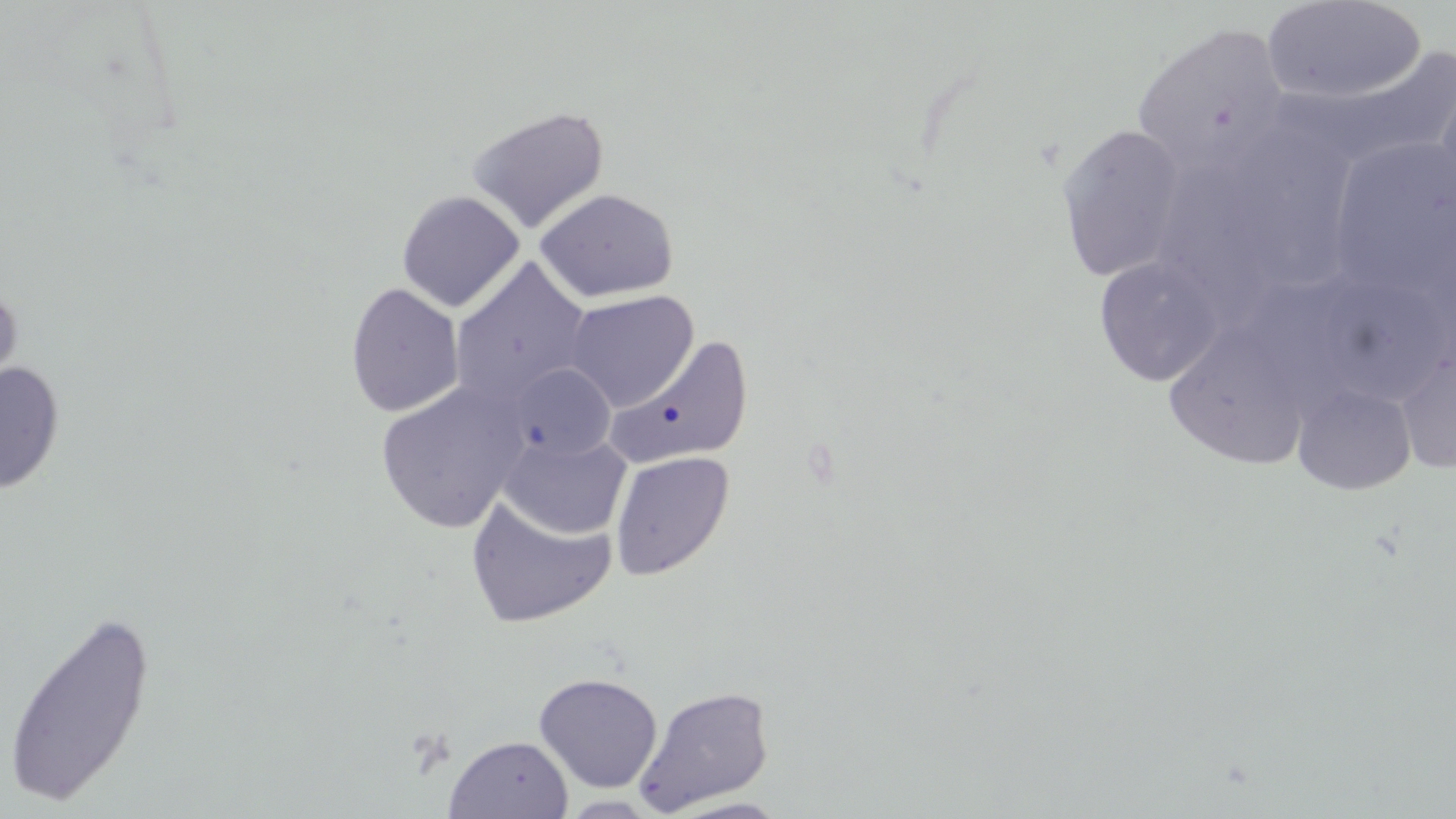
{
  "slide_level_diagnosis": "negative for blood parasites",
  "stain": "May-Grünwald-Giemsa",
  "preparation": "thin blood film",
  "image_size": "1456×819 pixels",
  "magnification": "1000x",
  "field_of_view": "one of a larger specimen",
  "modality": "optical microscopy",
  "uninfected_red_blood_cell_locations": "approximate bounding boxes as [x1, y1, x2, y2] in pixels: [1261, 1, 1426, 105], [1132, 23, 1290, 177], [1316, 42, 1456, 170], [1432, 70, 1456, 213], [466, 104, 611, 234], [1227, 119, 1362, 293], [1054, 123, 1190, 283], [1322, 136, 1453, 298], [1166, 165, 1296, 335], [535, 188, 679, 303], [396, 190, 525, 312], [1093, 256, 1225, 386], [450, 257, 593, 407], [0, 281, 23, 408], [345, 282, 464, 418], [564, 290, 699, 411], [1160, 328, 1318, 476], [607, 335, 754, 470], [1395, 343, 1456, 476], [0, 361, 65, 494], [504, 363, 616, 462], [375, 381, 529, 534], [1292, 382, 1417, 496], [499, 432, 631, 539], [609, 451, 734, 580], [465, 493, 617, 629], [2, 606, 159, 808], [533, 672, 663, 793], [634, 685, 775, 815], [444, 734, 574, 818], [558, 795, 662, 818], [664, 797, 793, 818]"
}